Locate and identify every blood parasite.
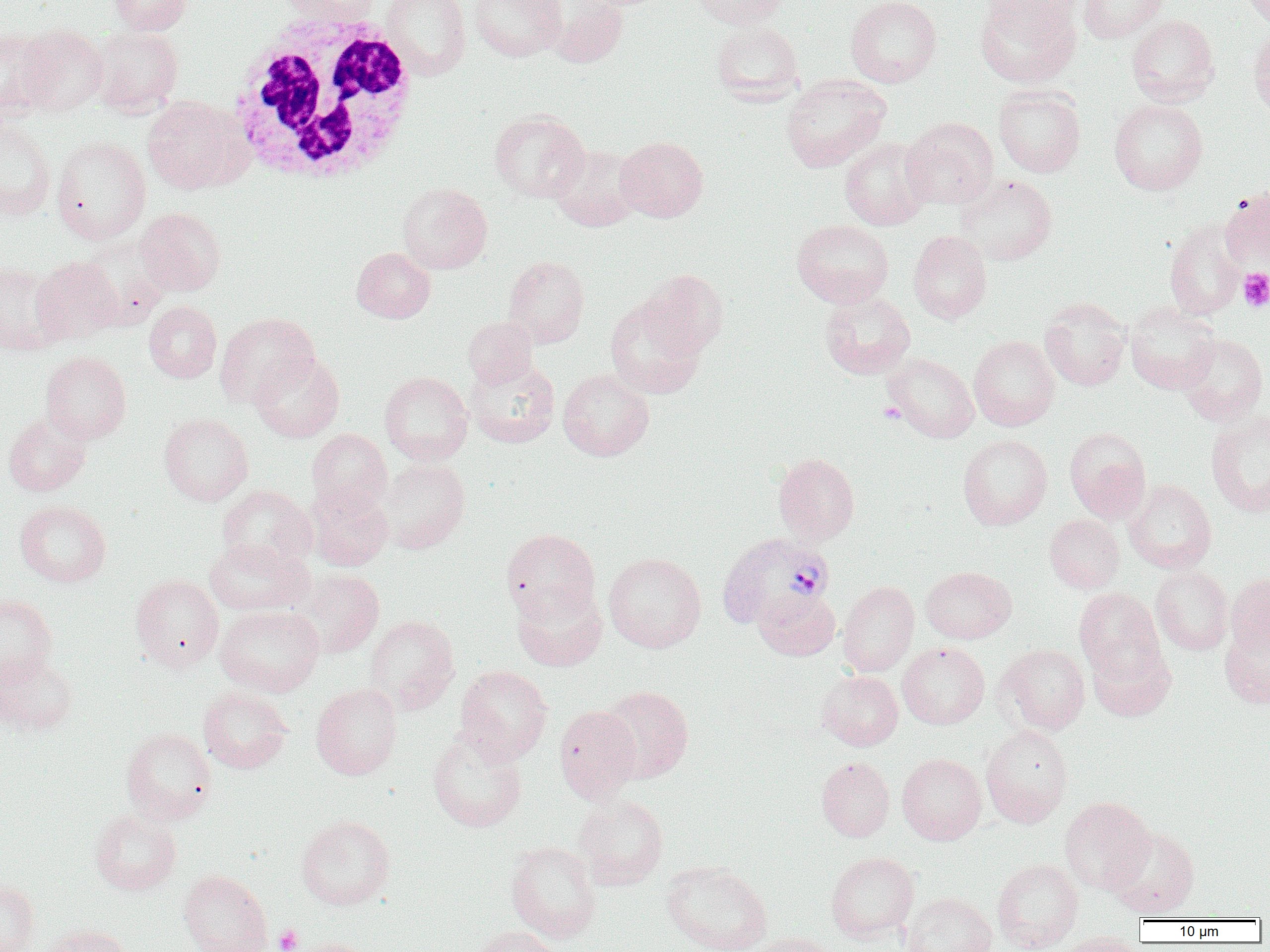
Approximate bounding boxes as named x1/y1/x2/y2 corners in pixels.
Plasmodium vivax-infected red blood cells: (x1=716, y1=532, x2=835, y2=631).
No Plasmodium falciparum, Plasmodium ovale, Plasmodium malariae, Babesia divergens, or Trypanosoma brucei observed.

Summary:
  - White blood cell locations: (x1=224, y1=11, x2=421, y2=186)
  - Uninfected red blood cell locations: (x1=110, y1=0, x2=192, y2=35), (x1=281, y1=0, x2=379, y2=23), (x1=381, y1=0, x2=471, y2=79), (x1=469, y1=0, x2=567, y2=62), (x1=691, y1=0, x2=791, y2=28), (x1=845, y1=0, x2=942, y2=87), (x1=980, y1=0, x2=1081, y2=24), (x1=1077, y1=0, x2=1170, y2=43), (x1=1242, y1=0, x2=1270, y2=28), (x1=548, y1=1, x2=628, y2=68), (x1=975, y1=1, x2=1081, y2=88), (x1=1126, y1=14, x2=1220, y2=107), (x1=711, y1=21, x2=804, y2=106), (x1=16, y1=24, x2=109, y2=116), (x1=89, y1=26, x2=183, y2=116), (x1=1248, y1=27, x2=1270, y2=121), (x1=0, y1=29, x2=53, y2=120), (x1=781, y1=74, x2=891, y2=173), (x1=993, y1=85, x2=1086, y2=178), (x1=142, y1=96, x2=247, y2=193), (x1=1109, y1=99, x2=1208, y2=195), (x1=489, y1=109, x2=590, y2=203), (x1=902, y1=117, x2=998, y2=209), (x1=0, y1=121, x2=56, y2=221), (x1=615, y1=136, x2=708, y2=222), (x1=51, y1=137, x2=151, y2=243), (x1=839, y1=137, x2=933, y2=230), (x1=549, y1=144, x2=642, y2=232), (x1=954, y1=174, x2=1057, y2=266), (x1=397, y1=182, x2=492, y2=274), (x1=1220, y1=188, x2=1270, y2=270), (x1=135, y1=208, x2=226, y2=296), (x1=792, y1=219, x2=893, y2=308), (x1=1164, y1=220, x2=1245, y2=320), (x1=908, y1=230, x2=992, y2=324), (x1=352, y1=247, x2=435, y2=323), (x1=503, y1=255, x2=590, y2=348), (x1=31, y1=256, x2=122, y2=344), (x1=0, y1=262, x2=63, y2=354), (x1=639, y1=269, x2=728, y2=357), (x1=819, y1=291, x2=916, y2=379), (x1=604, y1=297, x2=705, y2=399), (x1=1040, y1=298, x2=1131, y2=391), (x1=144, y1=301, x2=222, y2=383), (x1=1125, y1=302, x2=1220, y2=394), (x1=214, y1=312, x2=319, y2=409), (x1=462, y1=316, x2=537, y2=387), (x1=1178, y1=333, x2=1268, y2=425), (x1=969, y1=335, x2=1059, y2=431), (x1=40, y1=350, x2=131, y2=444), (x1=250, y1=352, x2=344, y2=442), (x1=882, y1=353, x2=979, y2=443), (x1=465, y1=357, x2=560, y2=448), (x1=558, y1=368, x2=654, y2=461), (x1=379, y1=371, x2=473, y2=465), (x1=1205, y1=411, x2=1270, y2=518), (x1=3, y1=412, x2=91, y2=496), (x1=159, y1=413, x2=253, y2=505), (x1=1065, y1=427, x2=1151, y2=523), (x1=306, y1=428, x2=392, y2=515), (x1=958, y1=434, x2=1052, y2=530), (x1=772, y1=452, x2=860, y2=545), (x1=377, y1=458, x2=470, y2=554), (x1=1124, y1=480, x2=1216, y2=573), (x1=306, y1=484, x2=393, y2=571), (x1=217, y1=485, x2=316, y2=569), (x1=15, y1=500, x2=111, y2=587), (x1=1044, y1=514, x2=1124, y2=593), (x1=501, y1=528, x2=600, y2=622), (x1=204, y1=538, x2=312, y2=616), (x1=603, y1=552, x2=706, y2=652), (x1=1150, y1=565, x2=1233, y2=655), (x1=920, y1=566, x2=1017, y2=643), (x1=295, y1=569, x2=384, y2=658), (x1=1226, y1=573, x2=1270, y2=655), (x1=130, y1=574, x2=224, y2=672), (x1=838, y1=581, x2=919, y2=676), (x1=511, y1=582, x2=607, y2=672), (x1=1074, y1=587, x2=1164, y2=680), (x1=754, y1=588, x2=840, y2=661), (x1=0, y1=593, x2=57, y2=686), (x1=215, y1=605, x2=324, y2=696), (x1=364, y1=615, x2=460, y2=715), (x1=1220, y1=622, x2=1270, y2=709), (x1=1087, y1=641, x2=1175, y2=722), (x1=897, y1=642, x2=990, y2=729), (x1=997, y1=644, x2=1090, y2=734), (x1=0, y1=652, x2=78, y2=735), (x1=455, y1=665, x2=553, y2=764), (x1=817, y1=670, x2=903, y2=751), (x1=311, y1=683, x2=402, y2=780), (x1=600, y1=685, x2=694, y2=783), (x1=197, y1=686, x2=294, y2=774), (x1=554, y1=706, x2=641, y2=802), (x1=981, y1=725, x2=1073, y2=827), (x1=121, y1=727, x2=217, y2=824), (x1=428, y1=728, x2=527, y2=832), (x1=897, y1=753, x2=987, y2=844), (x1=816, y1=757, x2=894, y2=841), (x1=573, y1=793, x2=669, y2=890), (x1=1060, y1=796, x2=1154, y2=894), (x1=90, y1=809, x2=181, y2=895), (x1=296, y1=814, x2=395, y2=910), (x1=1106, y1=826, x2=1200, y2=918), (x1=505, y1=841, x2=601, y2=942), (x1=825, y1=851, x2=919, y2=942), (x1=992, y1=858, x2=1083, y2=952), (x1=660, y1=860, x2=773, y2=952), (x1=177, y1=869, x2=272, y2=952), (x1=0, y1=879, x2=39, y2=952), (x1=902, y1=892, x2=996, y2=952), (x1=40, y1=924, x2=134, y2=952), (x1=473, y1=925, x2=564, y2=952), (x1=1059, y1=931, x2=1143, y2=952), (x1=749, y1=932, x2=839, y2=952), (x1=284, y1=936, x2=378, y2=952)
  - Platelet locations: (x1=1238, y1=269, x2=1270, y2=312), (x1=878, y1=402, x2=905, y2=424), (x1=274, y1=925, x2=302, y2=951)
  - Slide-level diagnosis: Plasmodium vivax
  - Preparation: thin blood smear
  - Magnification: 1000x
  - Image size: 1270×952 pixels
  - Field of view: one of a larger specimen
  - Modality: light microscopy